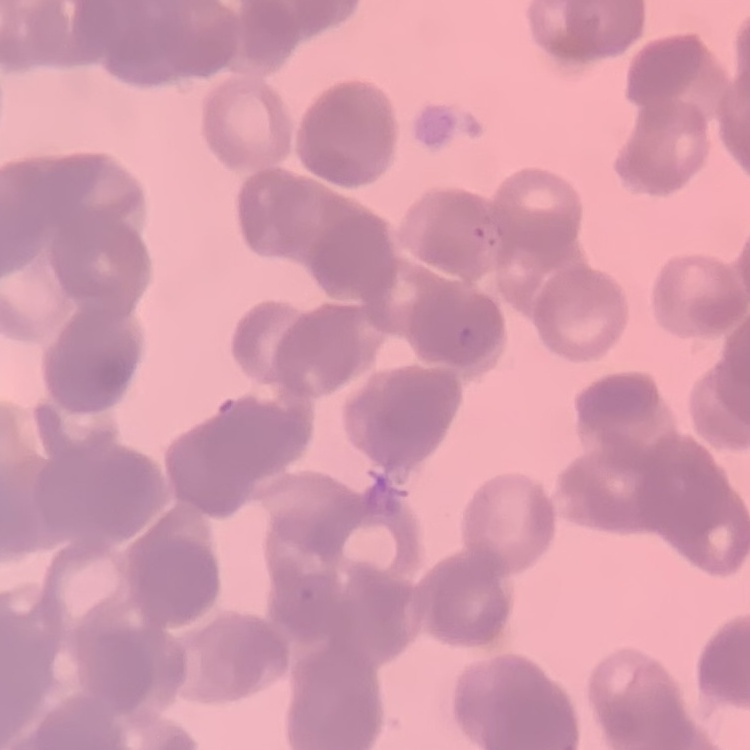

The erythrocytes exhibit rouleaux formation. Field's or Giemsa stain. Thin blood film. One tile cut from a larger photomicrograph.